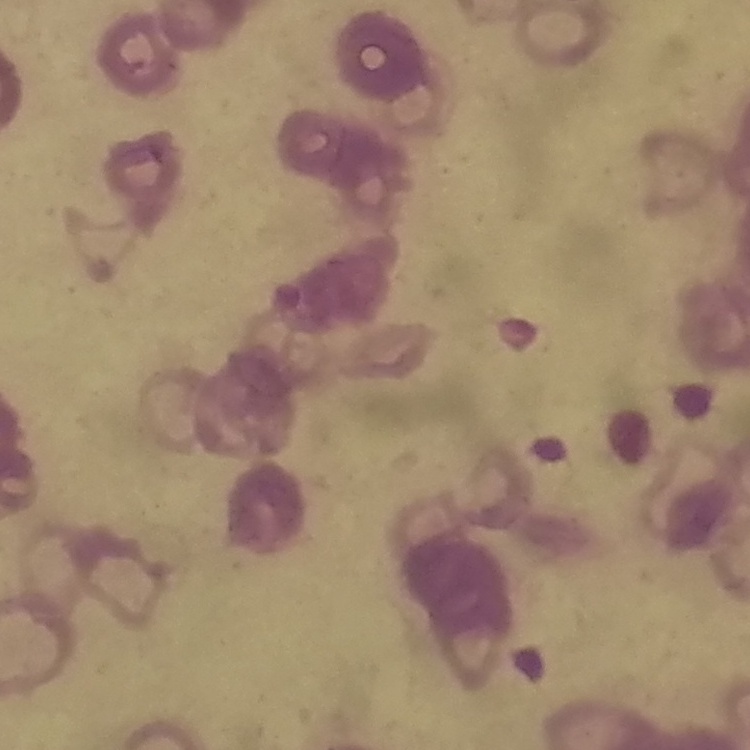 The red blood cells show rouleaux formation. Thin blood film. Stained with either Field's or Giemsa. One tile cut from a larger photomicrograph.